Report the malaria status of this cell.
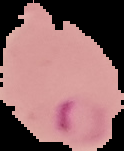

It is parasitized.

From a thin blood film. The area outside the segmented cell region is set to black. Image is 124×151 pixels.